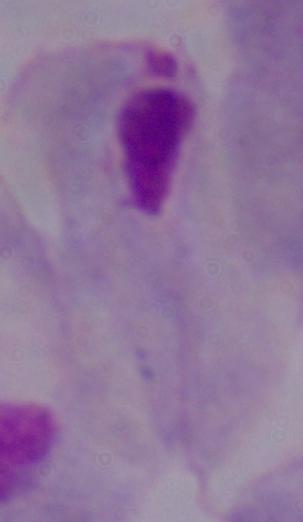

A trichomonad is seen. Micrograph. Captured at 1000x magnification.